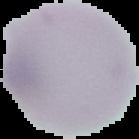 Segmented cell region on a black background. Image is 139×139 pixels. Malaria status: uninfected. From a thin blood smear.